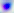
Summary:
  - Modality: photomicrograph
  - Identification: Toxoplasma gondii
  - Magnification: 400x